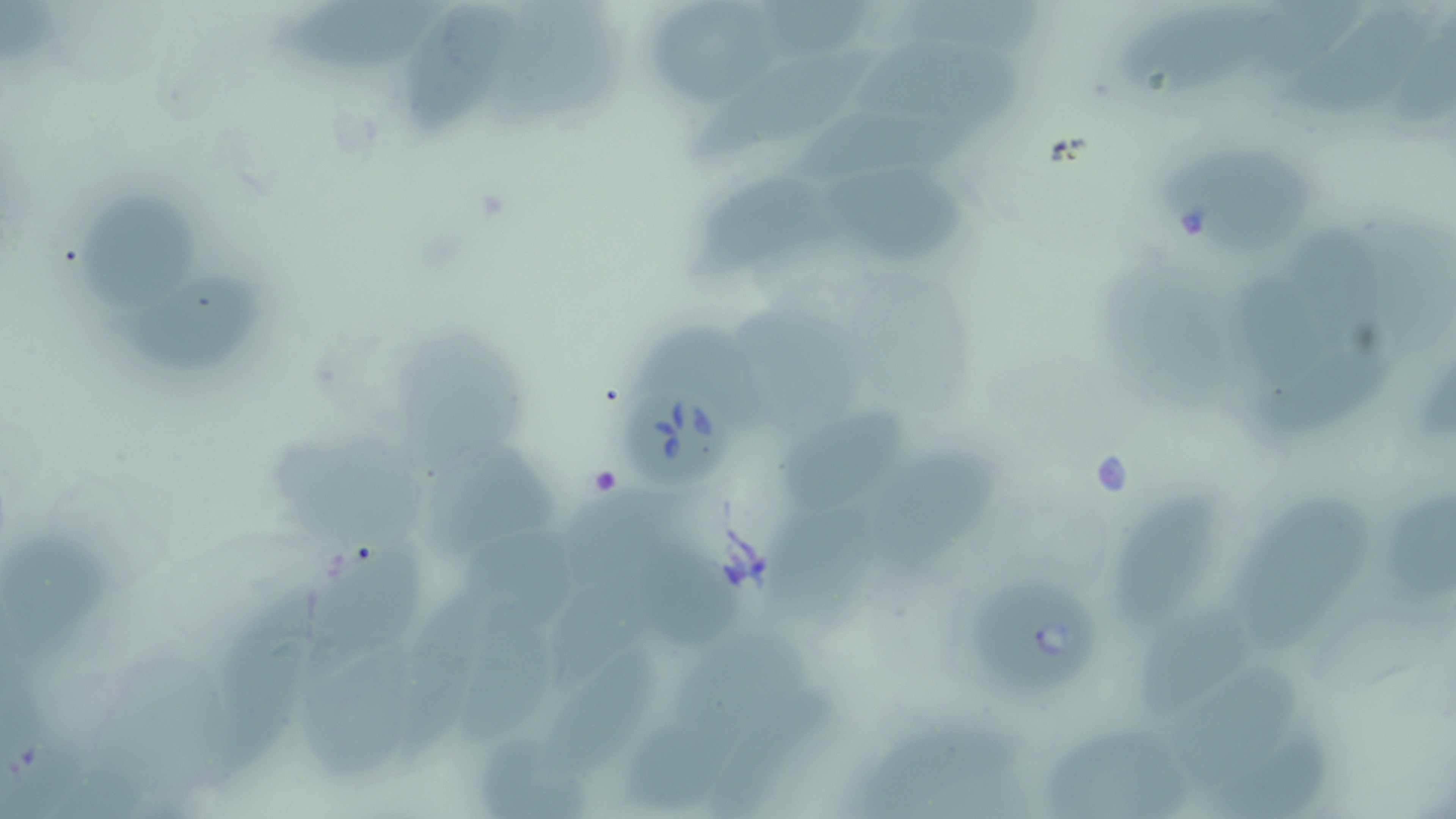

slide-level diagnosis = Babesia divergens
uninfected red blood cell locations = approximate bounding boxes as (x1, y1, x2, y2) in pixels: (283, 0, 453, 81), (500, 0, 631, 128), (894, 0, 1044, 68), (395, 2, 527, 147), (650, 5, 780, 108), (771, 5, 875, 54), (1115, 6, 1266, 109), (1247, 7, 1359, 82), (1288, 10, 1429, 128), (1409, 22, 1453, 141), (862, 39, 1019, 116), (696, 50, 879, 170), (807, 96, 984, 182), (1164, 157, 1319, 254), (688, 174, 823, 282), (843, 177, 975, 269), (80, 199, 197, 313), (1296, 219, 1367, 344), (1241, 269, 1330, 383), (135, 290, 260, 371), (751, 318, 875, 431), (646, 320, 770, 419), (402, 322, 539, 481), (1253, 340, 1401, 428), (787, 410, 902, 518), (283, 434, 429, 552), (436, 447, 556, 562), (866, 452, 999, 592), (1111, 481, 1224, 633), (1239, 485, 1384, 647), (1390, 491, 1456, 616), (583, 498, 692, 585), (763, 507, 875, 628), (472, 513, 582, 633), (9, 526, 114, 639), (312, 536, 429, 662), (645, 537, 743, 648), (552, 561, 661, 691), (217, 578, 322, 778), (395, 580, 509, 766), (1138, 592, 1258, 717), (472, 605, 563, 738), (678, 635, 812, 722), (298, 644, 426, 785), (556, 648, 664, 767), (1184, 648, 1314, 776), (709, 694, 827, 813), (630, 708, 740, 802), (1048, 715, 1190, 817), (857, 719, 1043, 818), (481, 734, 597, 818), (1211, 737, 1354, 819), (60, 757, 142, 819)
magnification = 1000x
modality = optical microscopy
stain = May-Grünwald-Giemsa
image size = 1456×819 pixels
preparation = thin blood film
field of view = single
Babesia divergens-infected red blood cell locations = approximate bounding boxes as (x1, y1, x2, y2) in pixels: (622, 383, 729, 485), (969, 578, 1099, 696)